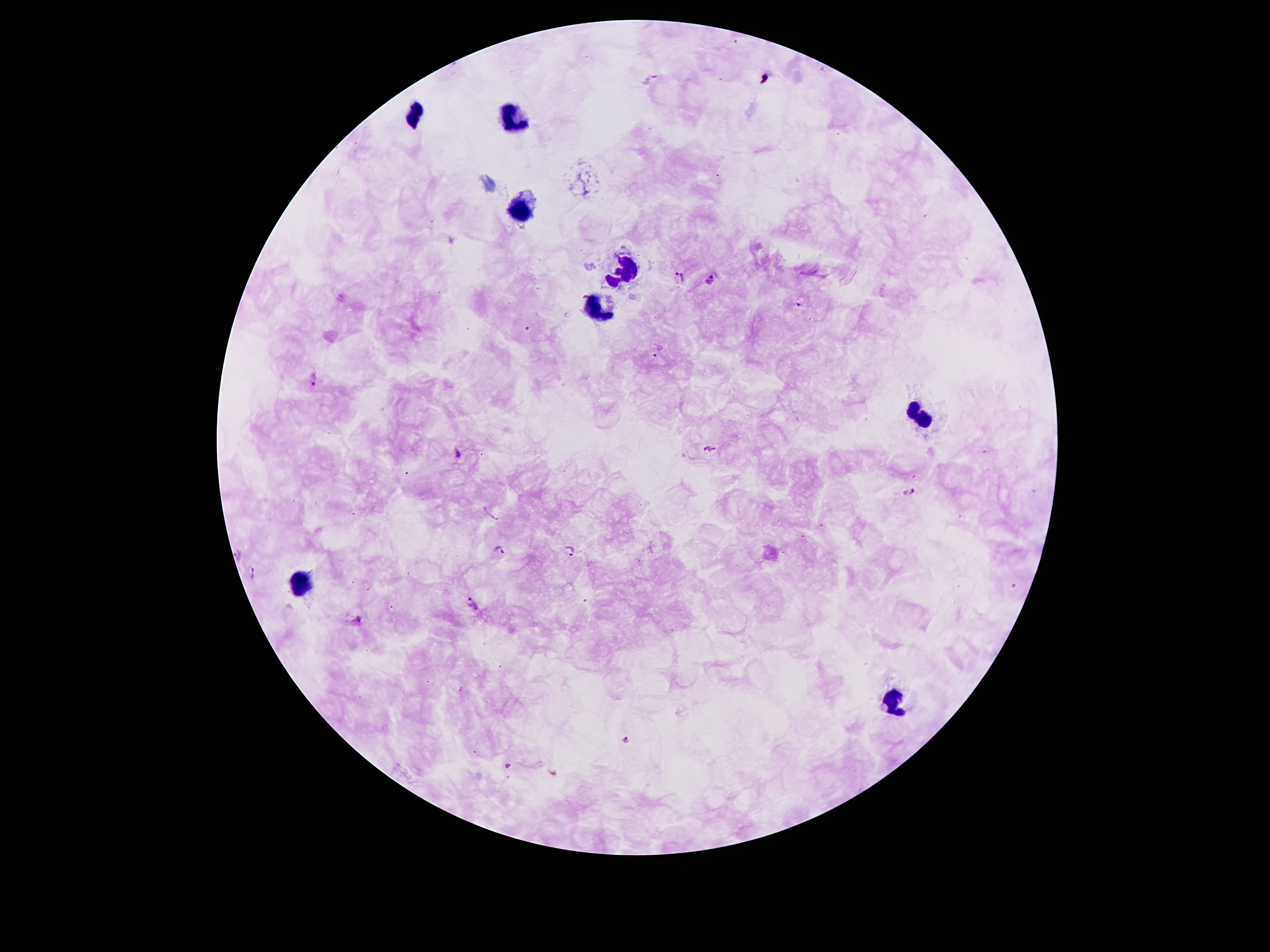

coordinate format = approximate centers as [x, y] in pixels
leukocyte locations = [417, 115], [516, 115], [516, 213], [626, 270], [594, 311], [920, 418], [303, 582], [893, 703]
malaria parasite locations = [680, 277], [711, 277], [798, 303], [656, 350], [316, 378], [709, 449], [457, 454], [908, 493], [499, 549], [570, 551], [236, 552], [254, 571], [475, 605], [358, 621], [625, 740]
image size = 1270×952 pixels
field of view = single
capture = smartphone through the microscope eyepiece
stain = Giemsa
magnification = 100x
patient malaria status = positive for Plasmodium falciparum
preparation = thick blood smear